Assess for malaria.
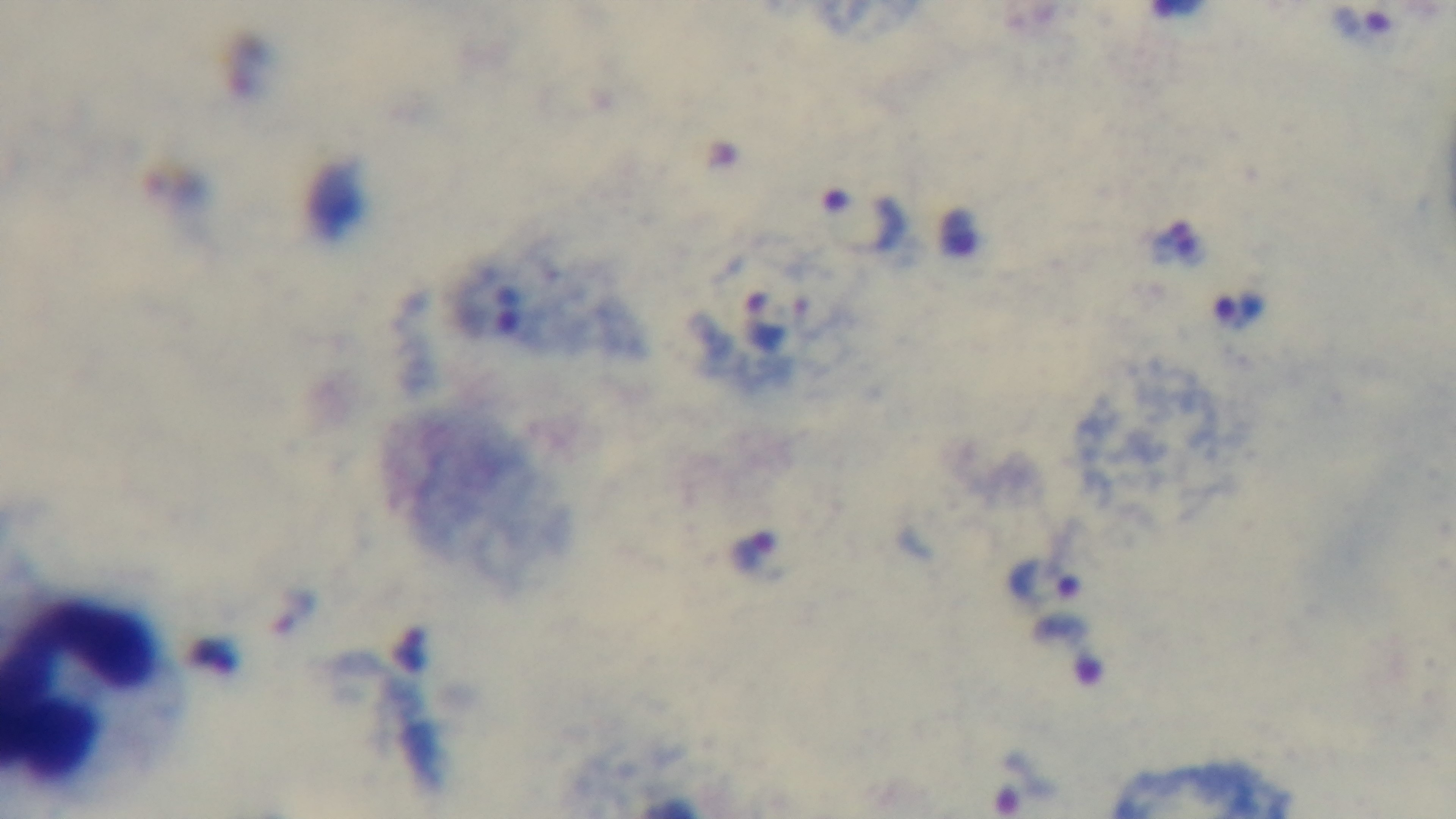

Infected.

100x oil-immersion objective. Giemsa-stained. Light microscopy. One field from the slide. Mounted 4K digital camera. Preparation: thick smear.